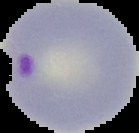

Summary:
  - Malaria status: parasitized
  - Preparation: thin blood smear
  - Image type: cell region segmented out of the field of view; surrounding area masked to black
  - Image size: 139×133 pixels